Report the malaria status of this cell.
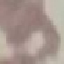

It is uninfected.

Cell patch, automatically extracted from a larger field of view and resized to 64 × 64 pixels. Acquired by smartphone through the microscope eyepiece. Thin blood smear. Giemsa-stained preparation.